State which parasite is depicted.
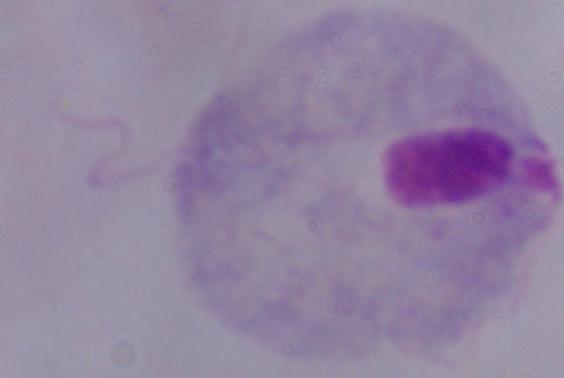

This is a trichomonad.

Summary:
  - Modality: photomicrograph
  - Magnification: 1000x